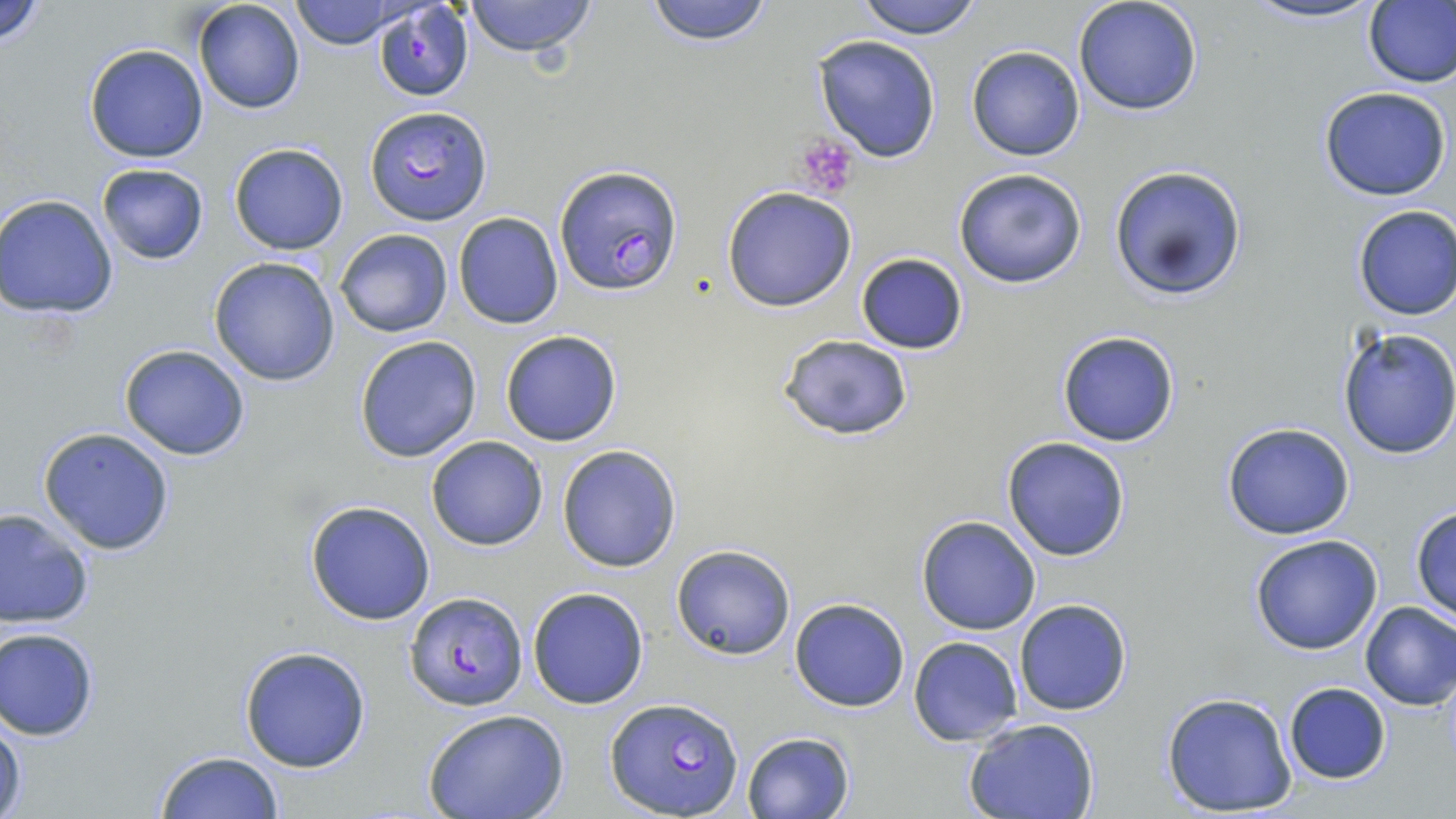
Summary:
  - Coordinate format: approximate bounding boxes as named x1/y1/x2/y2 corners in pixels
  - Uninfected red blood cell locations: (x1=0, y1=0, x2=49, y2=48), (x1=192, y1=0, x2=306, y2=114), (x1=289, y1=0, x2=408, y2=49), (x1=462, y1=0, x2=598, y2=58), (x1=643, y1=0, x2=776, y2=46), (x1=855, y1=0, x2=983, y2=40), (x1=1073, y1=0, x2=1204, y2=117), (x1=1238, y1=0, x2=1387, y2=25), (x1=1363, y1=1, x2=1456, y2=88), (x1=813, y1=35, x2=943, y2=163), (x1=84, y1=44, x2=208, y2=163), (x1=966, y1=46, x2=1086, y2=161), (x1=1318, y1=86, x2=1453, y2=202), (x1=228, y1=142, x2=350, y2=255), (x1=96, y1=163, x2=210, y2=266), (x1=1108, y1=164, x2=1248, y2=301), (x1=952, y1=167, x2=1088, y2=288), (x1=720, y1=187, x2=857, y2=312), (x1=1, y1=194, x2=120, y2=318), (x1=1351, y1=205, x2=1456, y2=321), (x1=453, y1=212, x2=563, y2=329), (x1=335, y1=228, x2=454, y2=338), (x1=856, y1=253, x2=969, y2=355), (x1=208, y1=256, x2=341, y2=387), (x1=1336, y1=327, x2=1456, y2=460), (x1=499, y1=329, x2=623, y2=446), (x1=1056, y1=330, x2=1181, y2=447), (x1=354, y1=335, x2=483, y2=463), (x1=777, y1=335, x2=916, y2=439), (x1=119, y1=345, x2=252, y2=461), (x1=1220, y1=422, x2=1356, y2=540), (x1=39, y1=426, x2=176, y2=556), (x1=426, y1=435, x2=548, y2=550), (x1=1001, y1=437, x2=1131, y2=560), (x1=557, y1=444, x2=682, y2=573), (x1=304, y1=498, x2=437, y2=626), (x1=0, y1=506, x2=95, y2=630), (x1=1411, y1=507, x2=1456, y2=618), (x1=915, y1=515, x2=1041, y2=635), (x1=1249, y1=533, x2=1384, y2=655), (x1=671, y1=543, x2=797, y2=660), (x1=527, y1=586, x2=649, y2=709), (x1=788, y1=599, x2=909, y2=712), (x1=1013, y1=600, x2=1133, y2=716), (x1=1359, y1=601, x2=1456, y2=711), (x1=0, y1=627, x2=101, y2=740), (x1=909, y1=636, x2=1025, y2=746), (x1=239, y1=644, x2=372, y2=773), (x1=1282, y1=681, x2=1392, y2=784), (x1=1160, y1=690, x2=1297, y2=816), (x1=0, y1=709, x2=27, y2=817), (x1=424, y1=711, x2=568, y2=819), (x1=963, y1=718, x2=1101, y2=819), (x1=742, y1=731, x2=854, y2=819), (x1=154, y1=750, x2=285, y2=819)
  - Plasmodium falciparum-infected red blood cell locations: (x1=372, y1=3, x2=473, y2=102), (x1=364, y1=107, x2=494, y2=227), (x1=554, y1=165, x2=684, y2=296), (x1=405, y1=592, x2=526, y2=712), (x1=604, y1=697, x2=743, y2=819)
  - Platelet locations: (x1=794, y1=134, x2=864, y2=199)
  - Slide-level diagnosis: Plasmodium falciparum
  - Magnification: 1000x
  - Stain: May-Grünwald-Giemsa
  - Image size: 1456×819 pixels
  - Field of view: single
  - Preparation: thin blood film
  - Modality: light microscopy